Locate every blood parasite and identify its species.
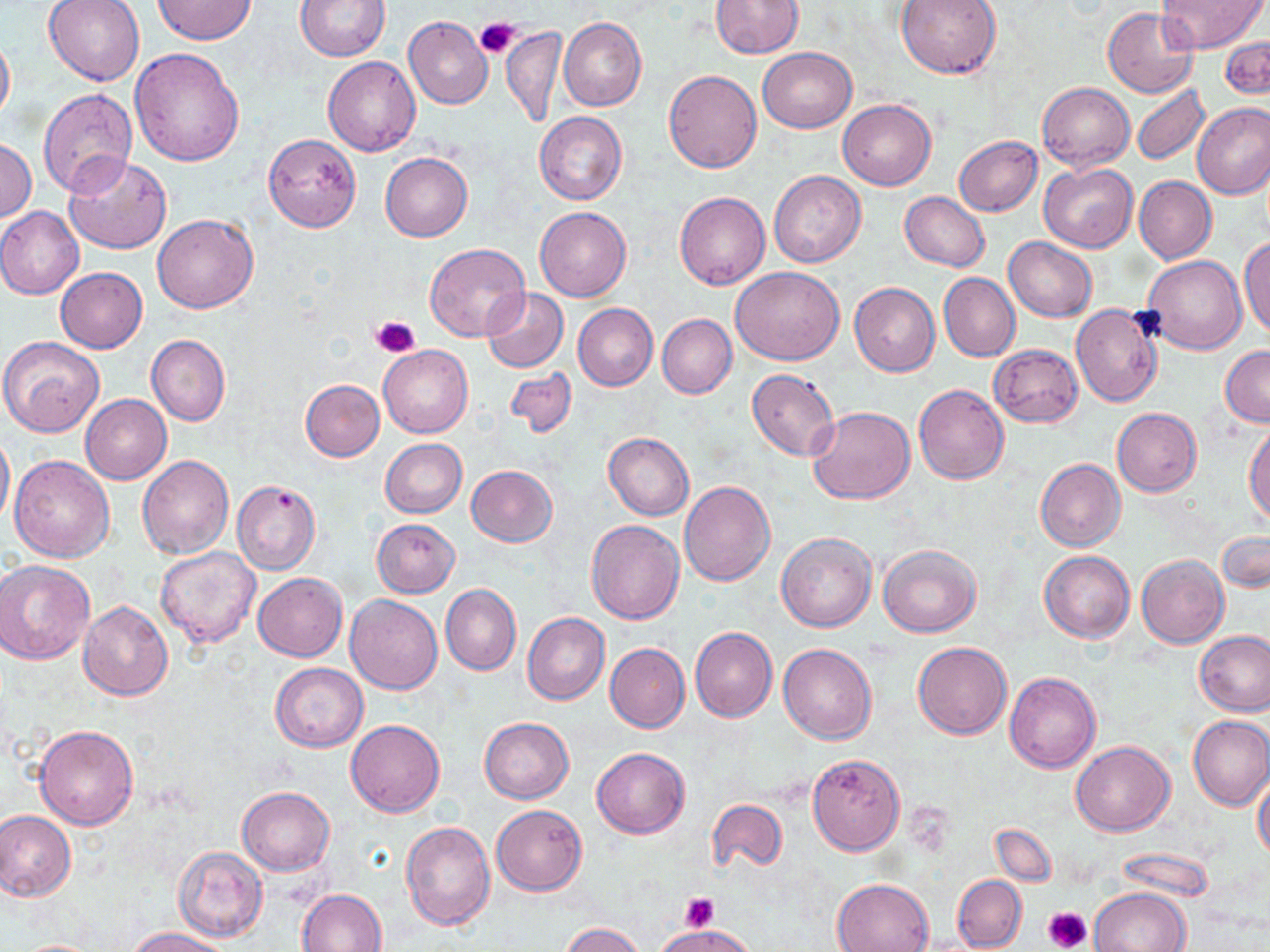
No blood parasites seen.

Summary:
  - Coordinate format: approximate bounding boxes as named x1/y1/x2/y2 corners in pixels
  - Uninfected red blood cell locations: (x1=42, y1=0, x2=145, y2=86), (x1=150, y1=0, x2=259, y2=46), (x1=295, y1=0, x2=389, y2=60), (x1=710, y1=0, x2=803, y2=57), (x1=895, y1=0, x2=1001, y2=79), (x1=1157, y1=1, x2=1265, y2=53), (x1=1103, y1=8, x2=1199, y2=97), (x1=403, y1=16, x2=493, y2=109), (x1=560, y1=18, x2=647, y2=111), (x1=502, y1=25, x2=568, y2=129), (x1=0, y1=27, x2=15, y2=129), (x1=1220, y1=36, x2=1270, y2=100), (x1=129, y1=47, x2=244, y2=165), (x1=758, y1=47, x2=856, y2=133), (x1=322, y1=56, x2=422, y2=157), (x1=663, y1=70, x2=761, y2=173), (x1=1038, y1=82, x2=1134, y2=170), (x1=1131, y1=84, x2=1210, y2=166), (x1=38, y1=88, x2=139, y2=200), (x1=837, y1=100, x2=936, y2=190), (x1=1192, y1=103, x2=1270, y2=198), (x1=534, y1=112, x2=627, y2=206), (x1=262, y1=132, x2=362, y2=232), (x1=954, y1=135, x2=1043, y2=216), (x1=1, y1=139, x2=37, y2=221), (x1=381, y1=152, x2=473, y2=242), (x1=64, y1=154, x2=174, y2=254), (x1=1039, y1=164, x2=1137, y2=253), (x1=769, y1=170, x2=866, y2=268), (x1=1134, y1=176, x2=1216, y2=264), (x1=675, y1=192, x2=770, y2=290), (x1=899, y1=192, x2=990, y2=271), (x1=0, y1=206, x2=83, y2=299), (x1=535, y1=206, x2=631, y2=301), (x1=152, y1=213, x2=260, y2=314), (x1=1004, y1=237, x2=1097, y2=321), (x1=1239, y1=238, x2=1270, y2=341), (x1=423, y1=243, x2=532, y2=344), (x1=1141, y1=255, x2=1246, y2=355), (x1=731, y1=265, x2=844, y2=364), (x1=55, y1=267, x2=148, y2=353), (x1=938, y1=273, x2=1020, y2=362), (x1=849, y1=282, x2=940, y2=376), (x1=482, y1=288, x2=568, y2=372), (x1=573, y1=303, x2=657, y2=390), (x1=1071, y1=303, x2=1164, y2=407), (x1=658, y1=314, x2=736, y2=399), (x1=146, y1=334, x2=230, y2=426), (x1=1, y1=336, x2=104, y2=437), (x1=989, y1=344, x2=1083, y2=426), (x1=378, y1=345, x2=473, y2=438), (x1=1220, y1=345, x2=1270, y2=426), (x1=504, y1=367, x2=577, y2=438), (x1=748, y1=370, x2=840, y2=461), (x1=300, y1=379, x2=385, y2=461), (x1=913, y1=383, x2=1009, y2=484), (x1=81, y1=394, x2=172, y2=484), (x1=808, y1=406, x2=915, y2=505), (x1=1111, y1=408, x2=1201, y2=497), (x1=1245, y1=423, x2=1270, y2=525), (x1=0, y1=427, x2=15, y2=528), (x1=603, y1=432, x2=694, y2=520), (x1=381, y1=439, x2=467, y2=518), (x1=8, y1=454, x2=114, y2=563), (x1=138, y1=454, x2=233, y2=559), (x1=1036, y1=458, x2=1126, y2=551), (x1=467, y1=465, x2=557, y2=546), (x1=230, y1=479, x2=320, y2=575), (x1=679, y1=480, x2=775, y2=586), (x1=372, y1=518, x2=460, y2=597), (x1=586, y1=519, x2=684, y2=624), (x1=1217, y1=529, x2=1269, y2=593), (x1=777, y1=533, x2=876, y2=632), (x1=878, y1=544, x2=981, y2=637), (x1=156, y1=547, x2=262, y2=649), (x1=1039, y1=550, x2=1135, y2=642), (x1=1136, y1=554, x2=1228, y2=648), (x1=0, y1=559, x2=96, y2=665), (x1=253, y1=572, x2=347, y2=661), (x1=440, y1=584, x2=521, y2=675), (x1=345, y1=595, x2=442, y2=694), (x1=78, y1=600, x2=172, y2=701), (x1=522, y1=612, x2=609, y2=704), (x1=690, y1=626, x2=777, y2=722), (x1=1195, y1=629, x2=1270, y2=716), (x1=913, y1=641, x2=1011, y2=739), (x1=605, y1=643, x2=689, y2=733), (x1=779, y1=644, x2=877, y2=744), (x1=270, y1=662, x2=367, y2=752), (x1=1004, y1=671, x2=1102, y2=774), (x1=1188, y1=716, x2=1270, y2=811), (x1=479, y1=717, x2=574, y2=804), (x1=346, y1=719, x2=445, y2=816), (x1=35, y1=724, x2=139, y2=830), (x1=1071, y1=740, x2=1174, y2=836), (x1=591, y1=746, x2=689, y2=839), (x1=807, y1=753, x2=905, y2=854), (x1=1252, y1=771, x2=1270, y2=862), (x1=237, y1=786, x2=334, y2=875), (x1=707, y1=798, x2=787, y2=874), (x1=491, y1=805, x2=587, y2=895), (x1=0, y1=810, x2=75, y2=903), (x1=400, y1=820, x2=496, y2=930), (x1=989, y1=823, x2=1058, y2=886), (x1=172, y1=846, x2=268, y2=942), (x1=952, y1=874, x2=1027, y2=951), (x1=832, y1=878, x2=934, y2=952), (x1=1090, y1=888, x2=1190, y2=952), (x1=297, y1=889, x2=388, y2=952), (x1=561, y1=922, x2=645, y2=952), (x1=656, y1=924, x2=755, y2=952), (x1=129, y1=927, x2=233, y2=952), (x1=12, y1=938, x2=108, y2=951)
  - Platelet locations: (x1=475, y1=20, x2=521, y2=61), (x1=371, y1=315, x2=419, y2=357), (x1=680, y1=893, x2=720, y2=930), (x1=1044, y1=905, x2=1093, y2=951)
  - Slide-level diagnosis: no evidence of blood parasites
  - Magnification: 1000x
  - Preparation: thin blood film
  - Field of view: single
  - Modality: optical microscopy
  - Image size: 1270×952 pixels
  - Stain: May-Grünwald-Giemsa